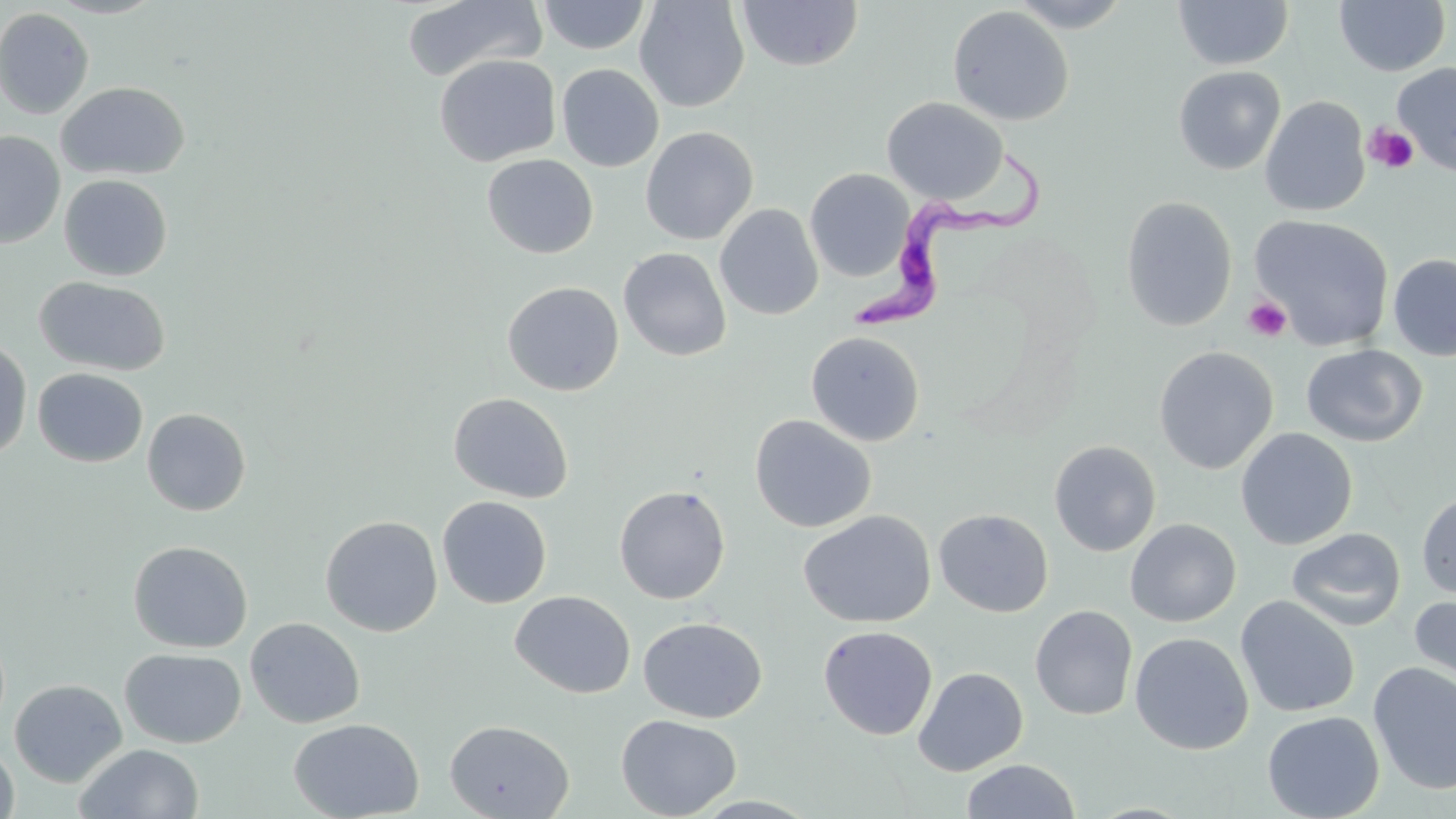
slide-level diagnosis = Trypanosoma brucei
magnification = 1000x
modality = light microscopy
stain = May-Grünwald-Giemsa
field of view = single
Trypanosoma brucei locations = approximate bounding boxes as named x1/y1/x2/y2 corners in pixels: (x1=850, y1=151, x2=1044, y2=337)
platelet locations = approximate bounding boxes as named x1/y1/x2/y2 corners in pixels: (x1=1364, y1=123, x2=1418, y2=174), (x1=1242, y1=296, x2=1292, y2=342)
uninfected red blood cell locations = approximate bounding boxes as named x1/y1/x2/y2 corners in pixels: (x1=46, y1=0, x2=166, y2=18), (x1=537, y1=0, x2=651, y2=55), (x1=634, y1=0, x2=750, y2=112), (x1=1007, y1=0, x2=1135, y2=32), (x1=1172, y1=0, x2=1294, y2=70), (x1=402, y1=1, x2=548, y2=82), (x1=737, y1=1, x2=863, y2=72), (x1=1334, y1=1, x2=1451, y2=76), (x1=947, y1=5, x2=1075, y2=126), (x1=0, y1=7, x2=95, y2=119), (x1=434, y1=54, x2=561, y2=167), (x1=1392, y1=62, x2=1456, y2=176), (x1=556, y1=63, x2=664, y2=172), (x1=1173, y1=66, x2=1286, y2=175), (x1=56, y1=81, x2=190, y2=181), (x1=882, y1=96, x2=1009, y2=204), (x1=1260, y1=96, x2=1370, y2=217), (x1=640, y1=126, x2=758, y2=245), (x1=0, y1=131, x2=65, y2=248), (x1=482, y1=154, x2=599, y2=258), (x1=804, y1=168, x2=914, y2=281), (x1=59, y1=174, x2=173, y2=281), (x1=1120, y1=196, x2=1238, y2=332), (x1=714, y1=203, x2=824, y2=320), (x1=1249, y1=214, x2=1394, y2=351), (x1=618, y1=247, x2=731, y2=362), (x1=1387, y1=253, x2=1456, y2=362), (x1=35, y1=276, x2=171, y2=376), (x1=502, y1=281, x2=624, y2=396), (x1=806, y1=331, x2=925, y2=447), (x1=0, y1=337, x2=33, y2=461), (x1=1301, y1=343, x2=1427, y2=447), (x1=1153, y1=346, x2=1278, y2=475), (x1=32, y1=367, x2=148, y2=467), (x1=448, y1=392, x2=574, y2=503), (x1=141, y1=408, x2=251, y2=516), (x1=749, y1=415, x2=876, y2=533), (x1=1235, y1=427, x2=1358, y2=550), (x1=1048, y1=440, x2=1162, y2=557), (x1=613, y1=484, x2=731, y2=604), (x1=1416, y1=491, x2=1456, y2=599), (x1=437, y1=495, x2=552, y2=608), (x1=934, y1=509, x2=1053, y2=617), (x1=799, y1=510, x2=936, y2=628), (x1=320, y1=515, x2=443, y2=636), (x1=1125, y1=518, x2=1241, y2=628), (x1=1287, y1=527, x2=1406, y2=631), (x1=127, y1=540, x2=253, y2=653), (x1=510, y1=590, x2=635, y2=698), (x1=1408, y1=593, x2=1456, y2=696), (x1=1235, y1=596, x2=1360, y2=717), (x1=1030, y1=605, x2=1138, y2=721), (x1=245, y1=617, x2=365, y2=728), (x1=638, y1=617, x2=766, y2=723), (x1=818, y1=625, x2=937, y2=740), (x1=1129, y1=632, x2=1254, y2=755), (x1=119, y1=647, x2=246, y2=748), (x1=1368, y1=661, x2=1456, y2=795), (x1=913, y1=667, x2=1028, y2=776), (x1=9, y1=678, x2=127, y2=787), (x1=1262, y1=710, x2=1385, y2=819), (x1=616, y1=714, x2=741, y2=818), (x1=289, y1=717, x2=424, y2=819), (x1=444, y1=719, x2=575, y2=819), (x1=0, y1=742, x2=19, y2=818), (x1=74, y1=742, x2=205, y2=819), (x1=960, y1=759, x2=1081, y2=818)
image size = 1456×819 pixels
preparation = thin blood film